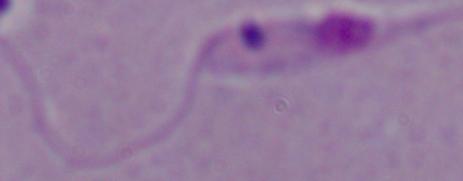 A Leishmania parasite is shown. Photomicrograph. 1000x magnification.